Identify the parasite.
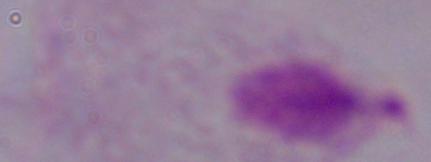
A trichomonad.

Summary:
  - Magnification: 1000x
  - Modality: photomicrograph